Classify this cell by malaria status.
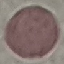

It is uninfected.

Summary:
  - Image type: automatically extracted cell patch, resized to 64 × 64 pixels
  - Preparation: thin smear
  - Capture: smartphone through the microscope eyepiece
  - Stain: Giemsa